Assess this cell for malaria.
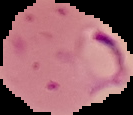

Parasitized.

The area outside the segmented cell region is set to black. From a thin blood smear. Image is 133×115 pixels.